Assess this cell for malaria.
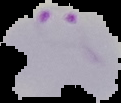
Parasitized.

image_type: segmented cell region on a black background
preparation: thin blood smear
image_size: 121×103 pixels